Identify the cell.
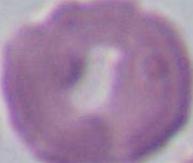

This is an erythrocyte.

magnification = 1000x
modality = micrograph